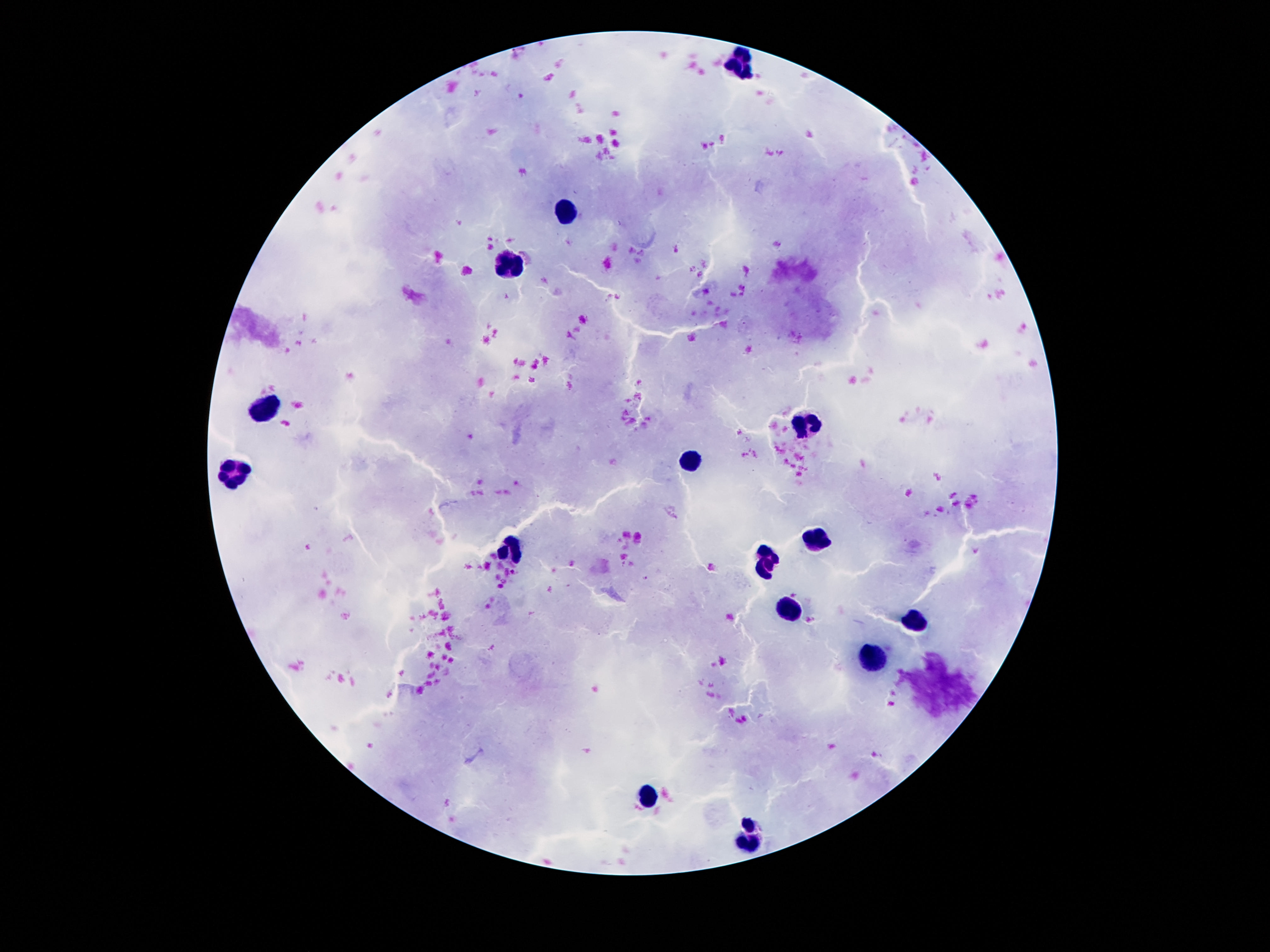
Approximate centers as (x, y) in pixels.
Summary:
  - Leukocyte locations: (740, 61), (566, 211), (512, 265), (268, 409), (810, 421), (694, 462), (238, 476), (812, 539), (508, 547), (768, 560), (790, 611), (918, 622), (874, 654), (648, 796), (750, 835)
  - Capture: smartphone camera through the microscope eyepiece
  - Image size: 1270×952 pixels
  - Field of view: one from this slide
  - Stain: Giemsa
  - Patient malaria status: uninfected
  - Preparation: thick peripheral-blood smear
  - Magnification: 100x